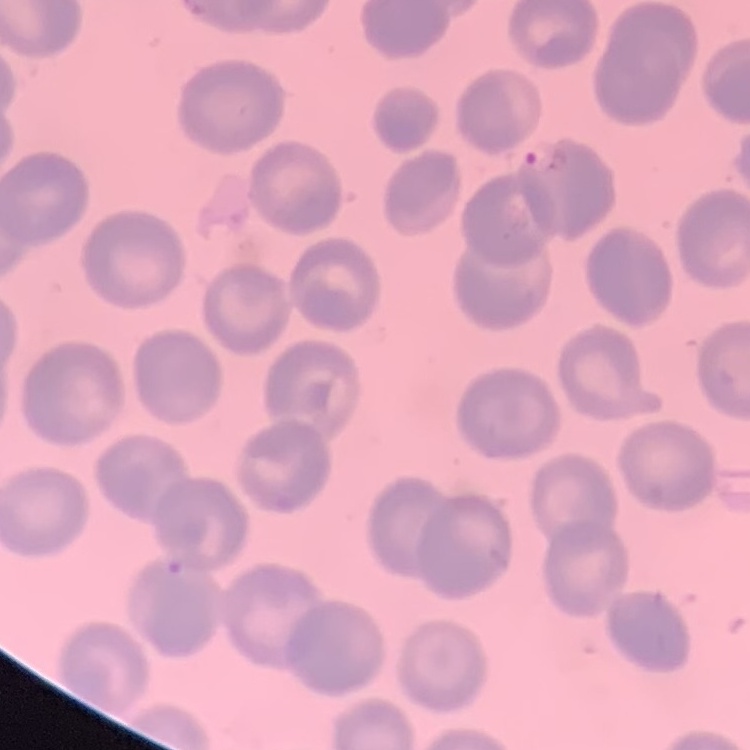
red blood cell morphology = no rouleaux formation
stain = Field's or Giemsa
preparation = thin blood smear
image type = one tile cut from a larger photomicrograph